Locate platelets.
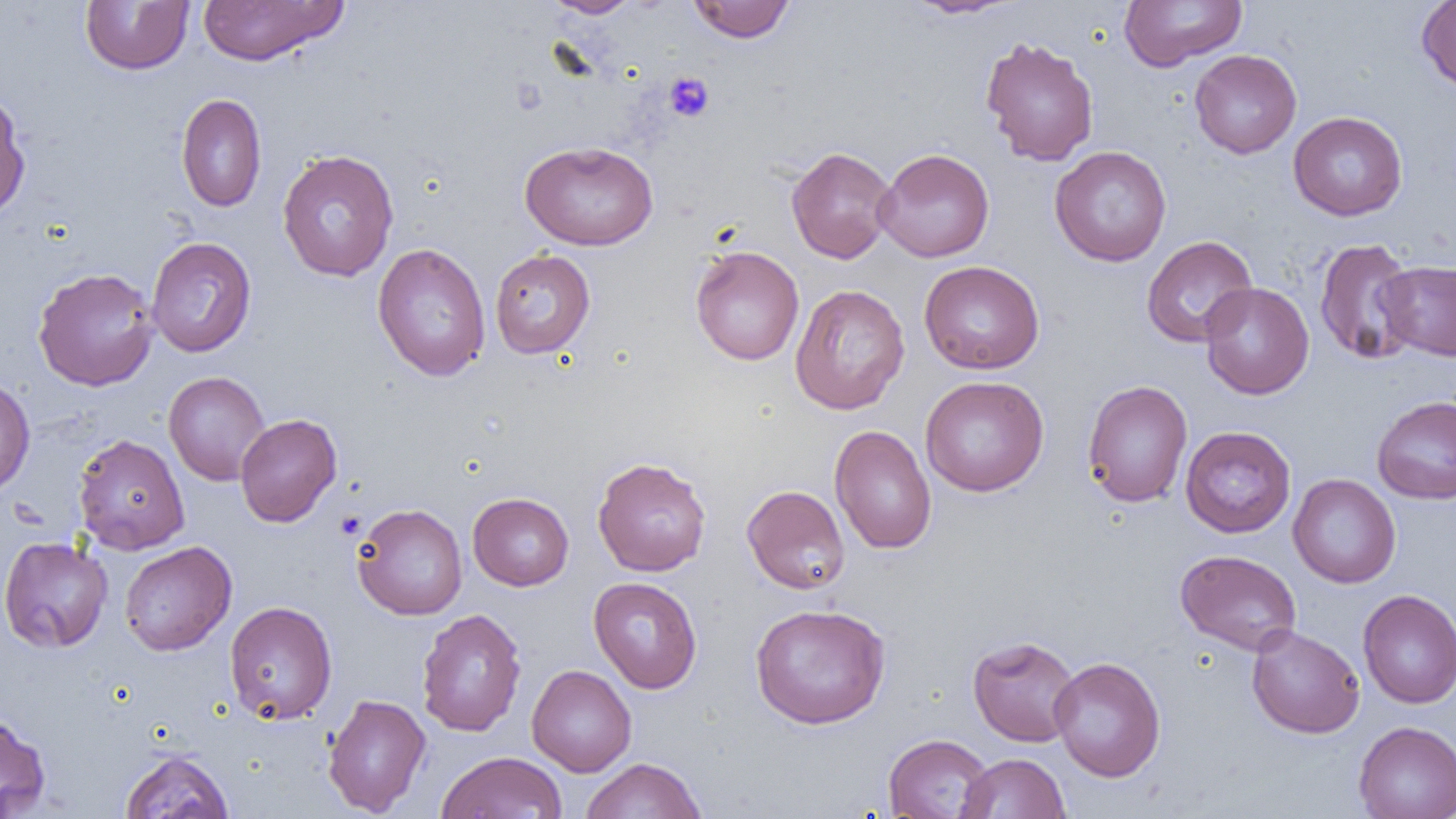

Approximate bounding boxes as [x1, y1, x2, y2] in pixels.
Platelets: [664, 72, 714, 122], [335, 510, 366, 539].

Summary:
  - Uninfected red blood cell locations: [80, 0, 194, 75], [198, 0, 348, 66], [544, 0, 643, 18], [687, 0, 796, 43], [903, 0, 1023, 19], [1417, 0, 1456, 94], [1119, 1, 1247, 71], [980, 36, 1099, 166], [1189, 49, 1302, 158], [0, 93, 32, 221], [175, 93, 267, 212], [1288, 111, 1408, 221], [519, 141, 658, 251], [786, 146, 897, 263], [1049, 146, 1172, 267], [875, 148, 995, 262], [277, 149, 399, 281], [1141, 235, 1258, 348], [146, 237, 257, 357], [1313, 237, 1421, 366], [372, 242, 491, 382], [689, 245, 804, 366], [490, 249, 595, 359], [919, 260, 1044, 374], [1377, 260, 1456, 361], [32, 266, 159, 392], [1199, 282, 1314, 399], [790, 284, 910, 415], [164, 371, 270, 485], [0, 373, 35, 497], [920, 375, 1049, 497], [1081, 379, 1193, 508], [1372, 395, 1456, 505], [235, 413, 341, 527], [829, 425, 937, 555], [1180, 425, 1296, 537], [73, 433, 190, 555], [592, 456, 711, 577], [1288, 473, 1401, 588], [742, 484, 851, 595], [467, 492, 574, 591], [352, 502, 467, 620], [0, 535, 114, 653], [119, 541, 236, 656], [1175, 549, 1302, 656], [588, 576, 703, 694], [1357, 589, 1456, 709], [224, 601, 338, 724], [750, 602, 891, 728], [416, 608, 526, 737], [1246, 624, 1365, 738], [967, 635, 1081, 746], [1049, 656, 1166, 782], [526, 664, 637, 776], [322, 694, 432, 816], [0, 712, 51, 818], [1353, 720, 1456, 819], [882, 733, 996, 818], [119, 749, 234, 819], [437, 751, 567, 819], [957, 753, 1070, 819], [581, 757, 707, 819]
  - Slide-level diagnosis: negative for blood parasites
  - Modality: light microscopy
  - Preparation: thin blood smear
  - Image size: 1456×819 pixels
  - Magnification: 1000x
  - Field of view: one of a larger specimen